Locate every blood parasite and identify its species.
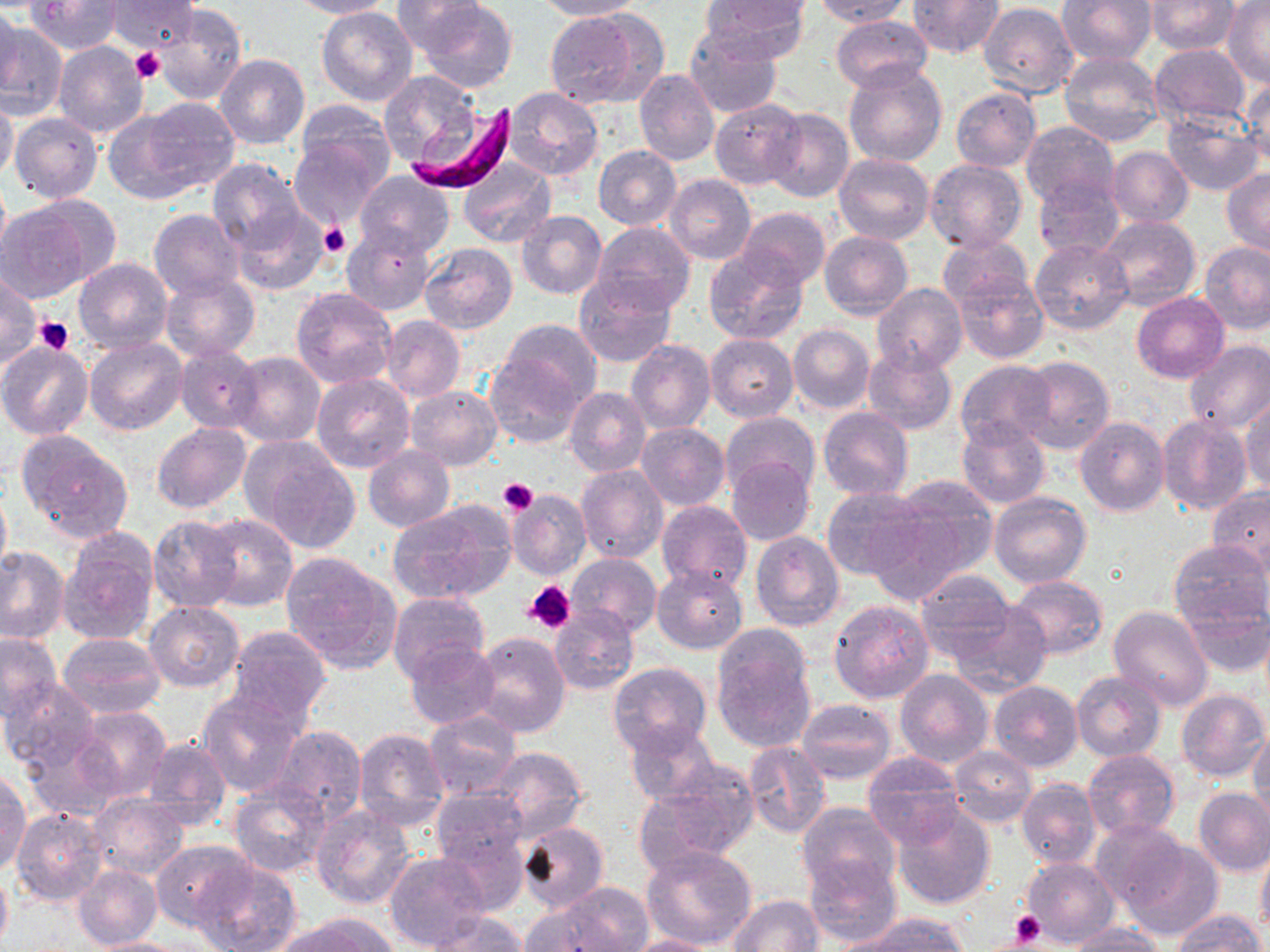
Approximate bounding boxes as (x1, y1, x2, y2) in pixels.
Plasmodium falciparum-infected red blood cells: (410, 101, 518, 193).
No Plasmodium ovale, Plasmodium malariae, Plasmodium vivax, Babesia divergens, or Trypanosoma brucei observed.

Summary:
  - Uninfected red blood cell locations: (26, 0, 122, 54), (289, 0, 395, 19), (419, 0, 518, 92), (700, 0, 812, 54), (811, 0, 911, 26), (907, 0, 1003, 59), (1146, 0, 1239, 55), (107, 1, 199, 51), (393, 1, 489, 56), (532, 1, 642, 21), (1056, 1, 1155, 67), (1224, 1, 1270, 86), (978, 3, 1077, 99), (0, 4, 21, 96), (153, 6, 244, 105), (317, 6, 419, 107), (545, 9, 662, 109), (832, 13, 933, 91), (0, 22, 68, 121), (684, 25, 781, 119), (53, 43, 148, 138), (1149, 43, 1251, 131), (1059, 51, 1163, 147), (214, 54, 309, 150), (843, 61, 947, 170), (634, 69, 721, 165), (378, 71, 481, 167), (1244, 77, 1270, 168), (502, 87, 602, 181), (951, 87, 1041, 171), (0, 95, 18, 184), (125, 97, 240, 195), (709, 99, 806, 190), (293, 100, 396, 194), (763, 107, 854, 203), (10, 113, 104, 203), (1161, 114, 1264, 196), (1020, 121, 1119, 209), (288, 132, 388, 227), (592, 145, 682, 229), (1105, 146, 1193, 227), (834, 152, 934, 246), (457, 158, 556, 248), (206, 159, 306, 258), (925, 159, 1027, 255), (1222, 168, 1270, 258), (354, 170, 455, 260), (664, 174, 756, 265), (1033, 175, 1126, 263), (2, 197, 109, 302), (737, 207, 830, 290), (231, 208, 331, 296), (148, 209, 245, 299), (515, 210, 607, 300), (1098, 215, 1200, 313), (592, 222, 695, 316), (341, 223, 434, 314), (819, 230, 913, 319), (938, 234, 1033, 312), (1030, 239, 1133, 335), (1201, 242, 1270, 335), (419, 244, 517, 335), (703, 248, 809, 345), (73, 257, 172, 354), (952, 271, 1048, 363), (572, 273, 676, 367), (0, 274, 40, 368), (160, 274, 260, 362), (870, 283, 966, 375), (290, 287, 398, 389), (1132, 293, 1228, 382), (380, 315, 464, 402), (493, 317, 601, 413), (788, 325, 874, 414), (705, 333, 798, 422), (84, 337, 187, 435), (626, 340, 716, 434), (1184, 340, 1270, 435), (0, 342, 94, 440), (175, 345, 264, 433), (861, 346, 958, 435), (484, 350, 589, 447), (230, 353, 326, 448), (1015, 356, 1117, 455), (957, 358, 1059, 450), (311, 373, 415, 473), (405, 385, 501, 470), (564, 388, 651, 476), (1240, 397, 1270, 496), (818, 406, 912, 499), (720, 411, 821, 502), (1156, 415, 1251, 516), (956, 417, 1050, 509), (1075, 417, 1169, 516), (151, 421, 251, 513), (635, 421, 731, 510), (15, 431, 134, 543), (242, 438, 360, 551), (364, 446, 454, 532), (726, 459, 816, 543), (576, 465, 669, 563), (879, 477, 998, 590), (0, 483, 11, 583), (822, 486, 929, 580), (1207, 486, 1270, 575), (505, 488, 592, 581), (990, 492, 1091, 589), (656, 498, 752, 592), (389, 500, 516, 605), (199, 513, 298, 611), (147, 514, 246, 613), (58, 531, 160, 646), (750, 531, 844, 631), (1167, 540, 1268, 632), (0, 546, 69, 642), (279, 552, 402, 673), (566, 553, 661, 639), (653, 564, 748, 654), (915, 573, 1021, 662), (1006, 574, 1108, 660), (387, 591, 491, 684), (1180, 599, 1269, 679), (829, 600, 935, 704), (946, 600, 1053, 694), (146, 601, 244, 691), (550, 606, 638, 695), (1108, 607, 1214, 711), (225, 625, 331, 726), (711, 629, 817, 753), (57, 631, 165, 719), (0, 632, 62, 723), (469, 632, 571, 739), (406, 642, 501, 729), (608, 662, 713, 756), (895, 668, 992, 769), (1072, 671, 1166, 762), (2, 678, 100, 772), (989, 680, 1082, 773), (197, 690, 306, 797), (1177, 690, 1269, 782), (796, 700, 896, 784), (69, 706, 172, 803), (422, 711, 521, 801), (624, 720, 722, 807), (271, 725, 368, 823), (20, 728, 124, 822), (1249, 728, 1270, 825), (354, 729, 449, 831), (141, 736, 232, 833), (743, 742, 830, 837), (481, 747, 590, 842), (949, 747, 1037, 826), (1082, 750, 1180, 840), (861, 751, 963, 847), (1, 771, 31, 876), (634, 774, 753, 872), (873, 778, 974, 884), (1017, 778, 1101, 869), (229, 783, 329, 878), (433, 788, 528, 870), (1193, 788, 1270, 876), (88, 793, 187, 878), (799, 802, 902, 899), (893, 802, 995, 911), (311, 804, 417, 909), (11, 808, 110, 908), (1091, 819, 1193, 912), (432, 821, 529, 917), (515, 821, 610, 914), (1115, 832, 1224, 939), (150, 838, 255, 931), (1256, 844, 1270, 938), (641, 846, 757, 950), (384, 852, 491, 952), (804, 855, 901, 946), (1021, 857, 1118, 947), (196, 861, 301, 952), (73, 864, 161, 950), (0, 867, 12, 950), (525, 883, 654, 952), (728, 894, 824, 952), (1171, 910, 1265, 952), (424, 911, 529, 951), (852, 914, 968, 951), (278, 915, 399, 952), (1064, 925, 1167, 952), (621, 934, 721, 952), (81, 937, 198, 951)
  - Platelet locations: (130, 46, 166, 85), (319, 221, 350, 260), (34, 317, 73, 355), (497, 478, 539, 515), (523, 580, 576, 634), (1009, 912, 1044, 948)
  - Slide-level diagnosis: Plasmodium falciparum
  - Field of view: one of a larger specimen
  - Preparation: thin blood film
  - Stain: May-Grünwald-Giemsa
  - Image size: 1270×952 pixels
  - Modality: light microscopy
  - Magnification: 1000x